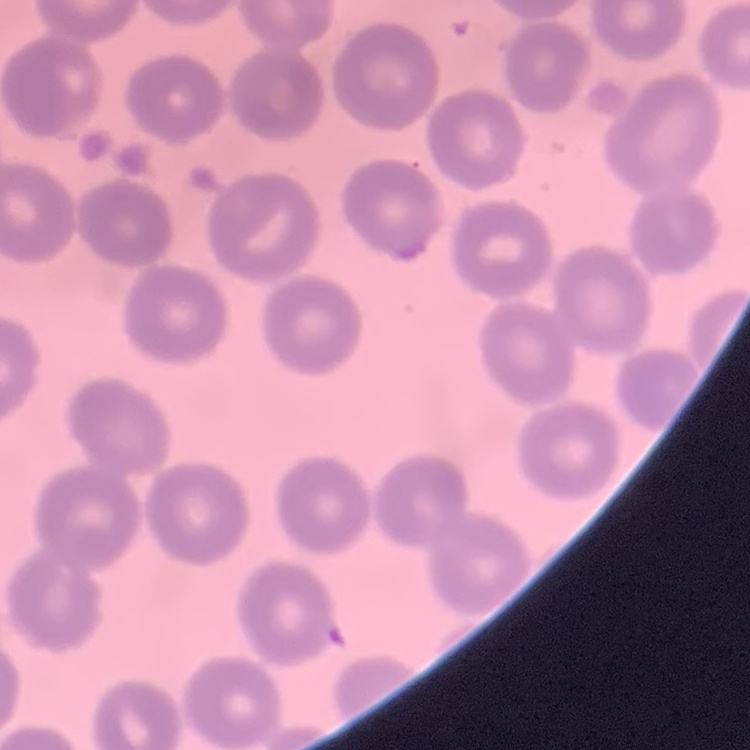

red blood cell morphology = no rouleaux formation
preparation = thin peripheral smear
stain = Field's or Giemsa
image type = one tile cut from a larger photomicrograph